Classify this cell by malaria status.
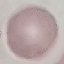

It is uninfected.

Summary:
  - Capture: smartphone through the microscope eyepiece
  - Stain: Giemsa
  - Preparation: thin blood smear
  - Image type: cell patch, automatically extracted from a larger field of view and resized to 64 × 64 pixels